Name the parasite shown.
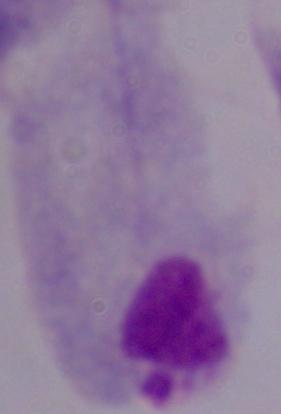
This is a trichomonad.

1000x magnification. Photomicrograph.